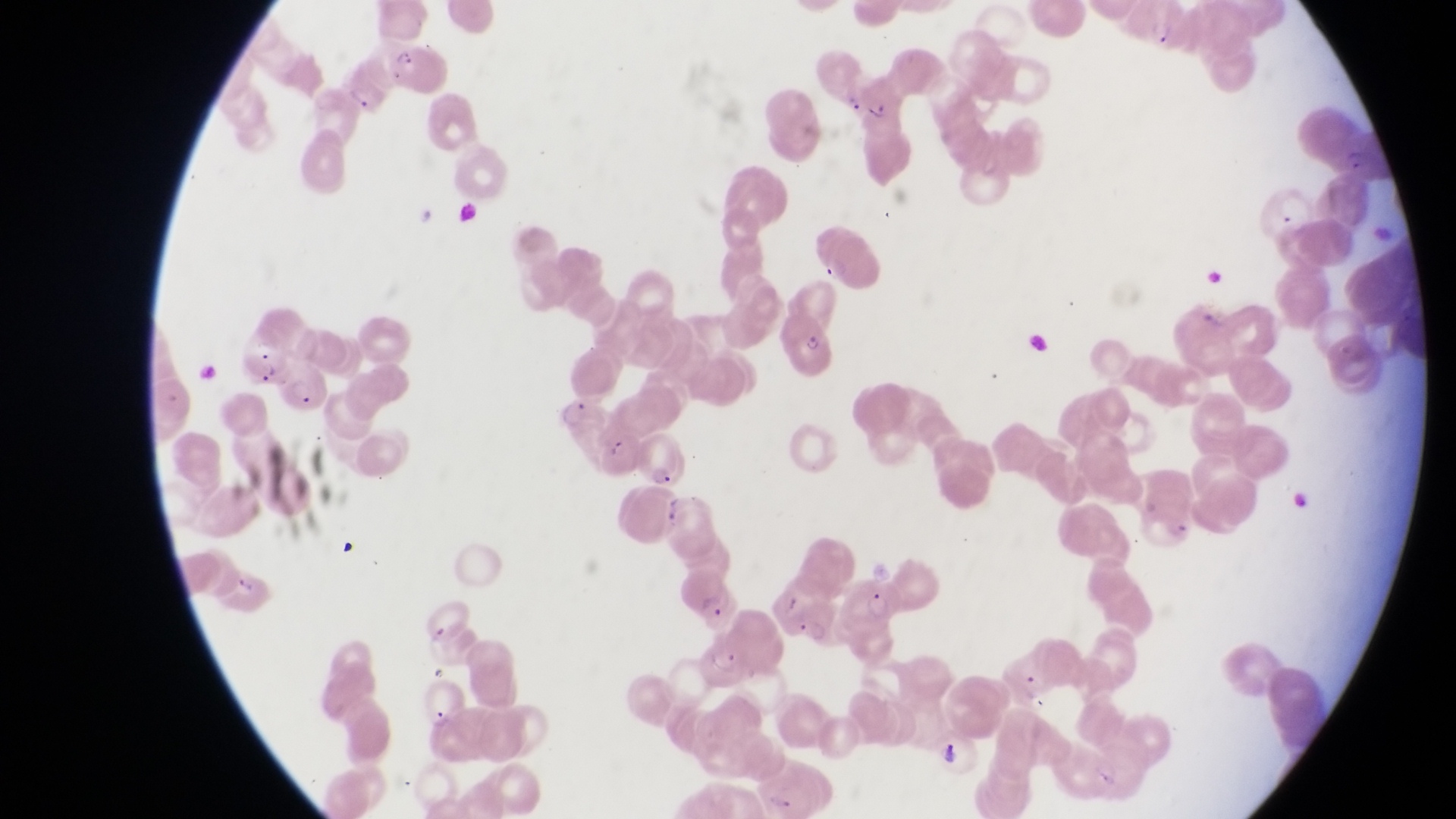

preparation: thin blood film
artifact_platelet_like_body_stain_precipitate_or_debris_locations: 'approximate bounding boxes as [left, top, right, bottom] in pixels: [412, 199, 435, 228], [1287, 486, 1314, 516]'
magnification: 1000x
country: Uganda
image_size: 1456×819 pixels
trophozoite_locations: 'approximate bounding boxes as [left, top, right, bottom] in pixels: [555, 400, 592, 429], [792, 617, 829, 646], [937, 737, 964, 769]'
parasitised_red_blood_cell_locations: 'approximate bounding boxes as [left, top, right, bottom] in pixels: [1128, 2, 1180, 43], [391, 39, 451, 94], [346, 66, 392, 115], [840, 74, 916, 183], [1310, 106, 1381, 180], [777, 314, 836, 377], [232, 328, 295, 386], [588, 435, 638, 481], [631, 436, 689, 489], [840, 573, 900, 631]'
field_of_view: single
capture: smartphone photograph through the eyepiece of an Olympus CX-23 microscope